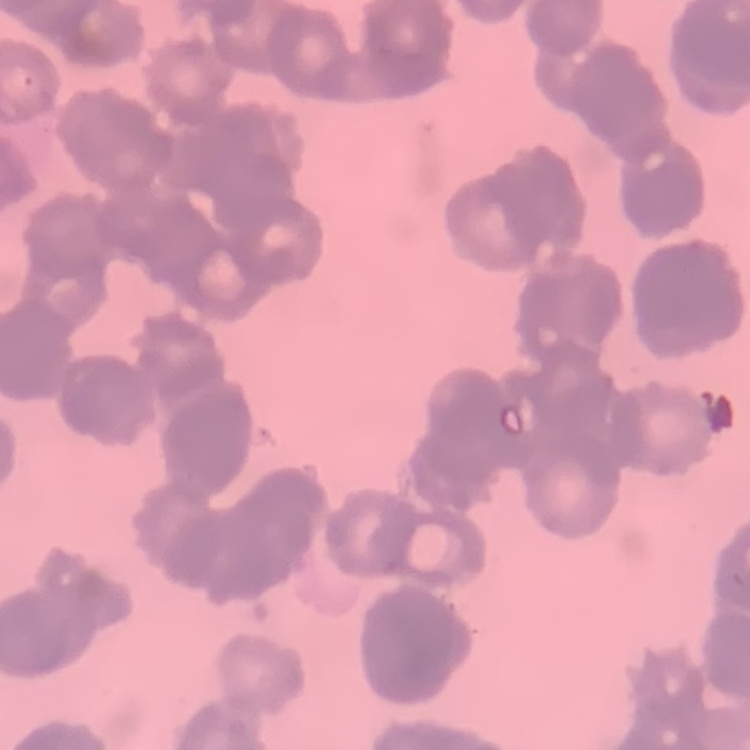

erythrocyte morphology = rouleaux formation
preparation = thin blood film
stain = Field's or Giemsa
image type = square crop of a larger photomicrograph